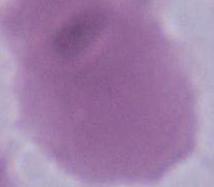

magnification = 1000x
modality = micrograph
identification = erythrocyte